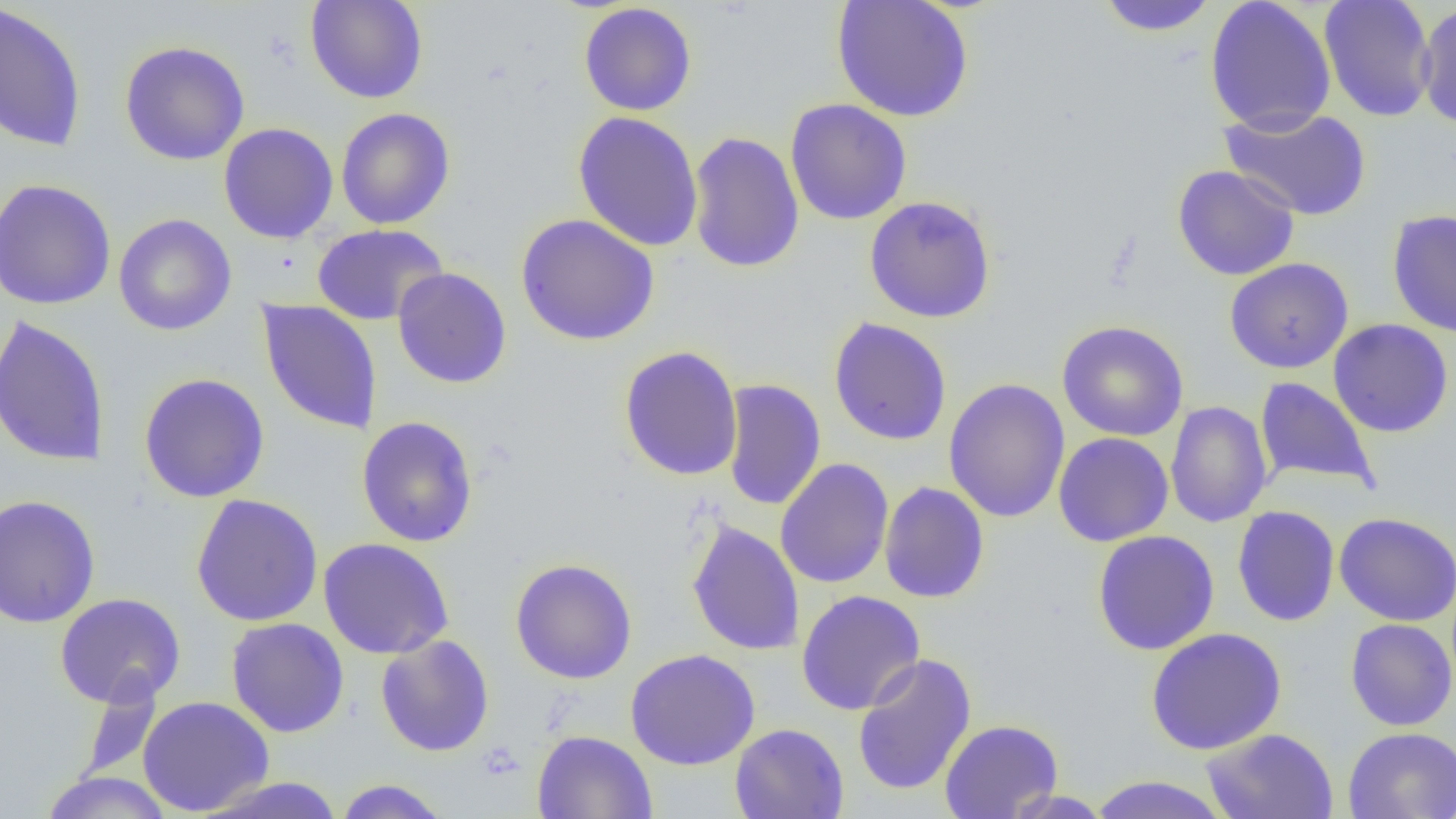
slide-level diagnosis = no evidence of blood parasites
uninfected red blood cell locations = approximate bounding boxes as [x1, y1, x2, y2] in pixels: [304, 0, 429, 104], [831, 0, 974, 122], [1096, 0, 1219, 37], [1204, 0, 1337, 135], [1318, 1, 1437, 122], [0, 2, 88, 152], [1416, 2, 1456, 130], [578, 3, 697, 116], [119, 40, 250, 165], [785, 98, 913, 225], [1219, 105, 1372, 220], [336, 107, 456, 230], [573, 111, 704, 252], [219, 122, 338, 244], [686, 131, 805, 274], [1172, 164, 1300, 281], [0, 178, 116, 310], [864, 195, 997, 323], [1387, 209, 1456, 337], [515, 213, 660, 346], [113, 214, 237, 336], [312, 224, 448, 326], [1224, 258, 1353, 373], [392, 267, 512, 389], [257, 300, 382, 435], [0, 314, 111, 468], [828, 317, 953, 446], [1328, 319, 1454, 438], [1057, 321, 1189, 441], [618, 345, 744, 481], [138, 373, 270, 503], [943, 377, 1070, 524], [1254, 377, 1380, 494], [721, 378, 826, 512], [1165, 400, 1272, 528], [356, 415, 478, 548], [1053, 432, 1174, 546], [774, 458, 894, 589], [878, 481, 990, 603], [191, 494, 323, 626], [0, 495, 101, 629], [1232, 505, 1340, 626], [1334, 512, 1456, 626], [686, 520, 805, 657], [1092, 529, 1220, 655], [317, 538, 455, 659], [510, 558, 638, 684], [796, 590, 926, 715], [54, 592, 186, 708], [226, 617, 349, 738], [1345, 618, 1456, 731], [1145, 628, 1286, 755], [375, 634, 494, 757], [626, 649, 761, 770], [851, 652, 978, 796], [78, 674, 162, 782], [137, 695, 275, 816], [939, 718, 1063, 818], [730, 723, 849, 819], [1342, 727, 1456, 818], [1201, 728, 1339, 819], [532, 730, 658, 819], [40, 771, 173, 818], [1087, 775, 1233, 819], [195, 776, 348, 818], [333, 779, 450, 818], [1000, 789, 1114, 818]
magnification = 1000x
modality = light microscopy
image size = 1456×819 pixels
field of view = single
preparation = thin blood smear